Report the malaria status of this cell.
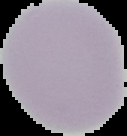
Uninfected.

preparation = thin blood smear
image size = 127×136 pixels
image type = segmented cell region with the area outside set to black